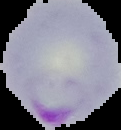
Summary:
  - Malaria status: parasitized
  - Image type: cell region segmented out of the field of view; surrounding area masked to black
  - Preparation: thin blood film
  - Image size: 121×130 pixels